Comment on the morphology of the erythrocytes.
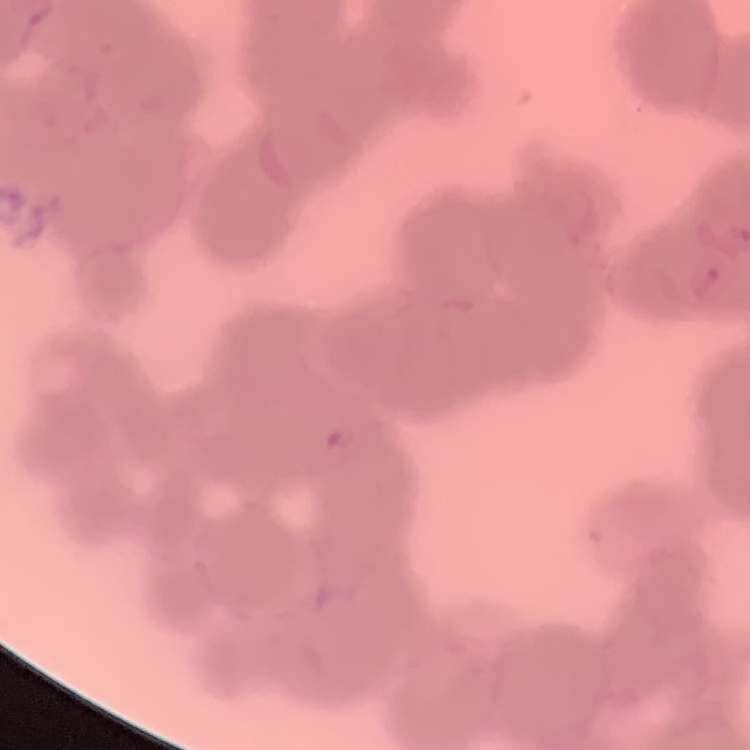

They show rouleaux formation.

Summary:
  - Preparation: thin peripheral smear
  - Image type: square crop of a larger photomicrograph
  - Stain: Field's or Giemsa